Outline each uninfected red blood cell.
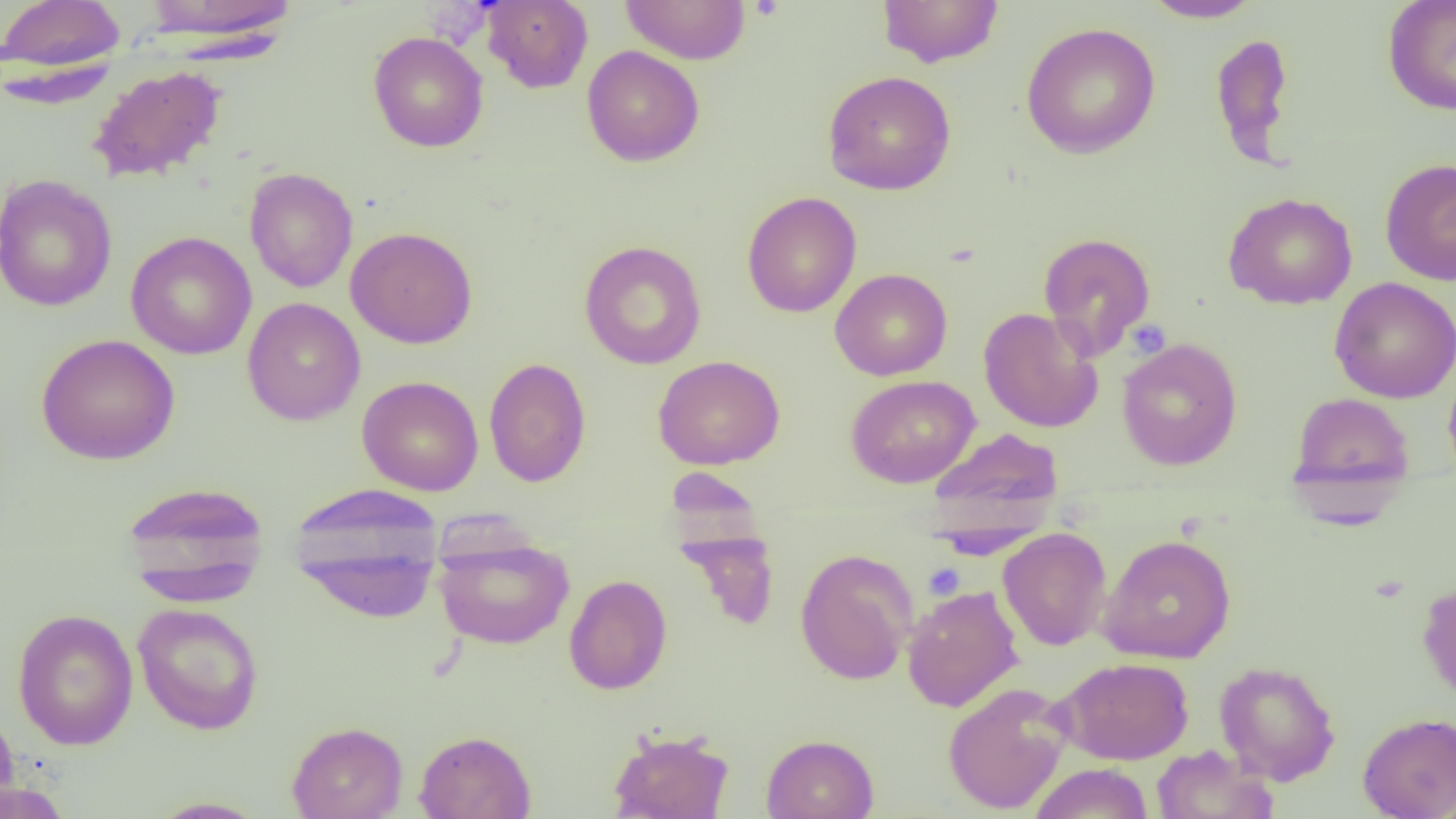
Approximate bounding boxes as (x1, y1, x2, y2) in pixels.
Uninfected red blood cells: (0, 0, 126, 78), (141, 0, 297, 40), (620, 0, 751, 65), (877, 0, 1004, 68), (1142, 0, 1264, 23), (1383, 0, 1456, 115), (482, 1, 593, 93), (1020, 22, 1161, 159), (368, 31, 488, 152), (1210, 32, 1295, 166), (582, 45, 704, 167), (88, 65, 226, 184), (822, 70, 956, 195), (1380, 158, 1456, 286), (244, 166, 358, 293), (0, 174, 117, 312), (742, 191, 862, 318), (1224, 191, 1358, 310), (346, 226, 477, 349), (126, 231, 257, 359), (1038, 232, 1156, 358), (579, 240, 707, 369), (830, 268, 952, 381), (1329, 276, 1456, 403), (242, 297, 365, 425), (978, 307, 1103, 433), (36, 333, 180, 465), (1116, 337, 1242, 471), (653, 355, 785, 470), (484, 357, 591, 487), (1443, 364, 1456, 486), (845, 374, 980, 488), (357, 375, 484, 496), (1288, 391, 1415, 510), (925, 427, 1064, 538), (120, 480, 270, 603), (289, 486, 445, 623), (676, 528, 780, 631), (998, 528, 1111, 651), (433, 532, 575, 650), (1098, 533, 1237, 663), (795, 548, 918, 685), (564, 574, 672, 695), (1417, 579, 1456, 706), (902, 584, 1024, 712), (133, 602, 264, 735), (12, 608, 139, 750), (1056, 657, 1194, 764), (1214, 661, 1341, 785), (943, 682, 1073, 815), (0, 706, 21, 815), (1357, 712, 1456, 818), (287, 721, 408, 819), (606, 727, 734, 819), (414, 730, 537, 819), (762, 733, 879, 819), (1151, 745, 1277, 819), (1029, 763, 1154, 819), (0, 779, 72, 819), (149, 797, 268, 818).

Summary:
  - Platelet locations: (923, 562, 965, 600)
  - Slide-level diagnosis: negative for blood parasites
  - Field of view: single
  - Image size: 1456×819 pixels
  - Magnification: 1000x
  - Modality: light microscopy
  - Preparation: thin blood smear